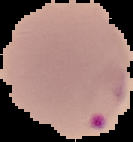

Summary:
  - Malaria status: parasitized
  - Image type: cell region segmented out of the field of view; surrounding area masked to black
  - Preparation: thin blood smear
  - Image size: 133×142 pixels